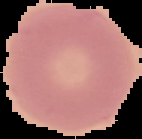
Summary:
  - Preparation: thin blood film
  - Image size: 142×139 pixels
  - Image type: segmented cell region on a black background
  - Malaria status: uninfected